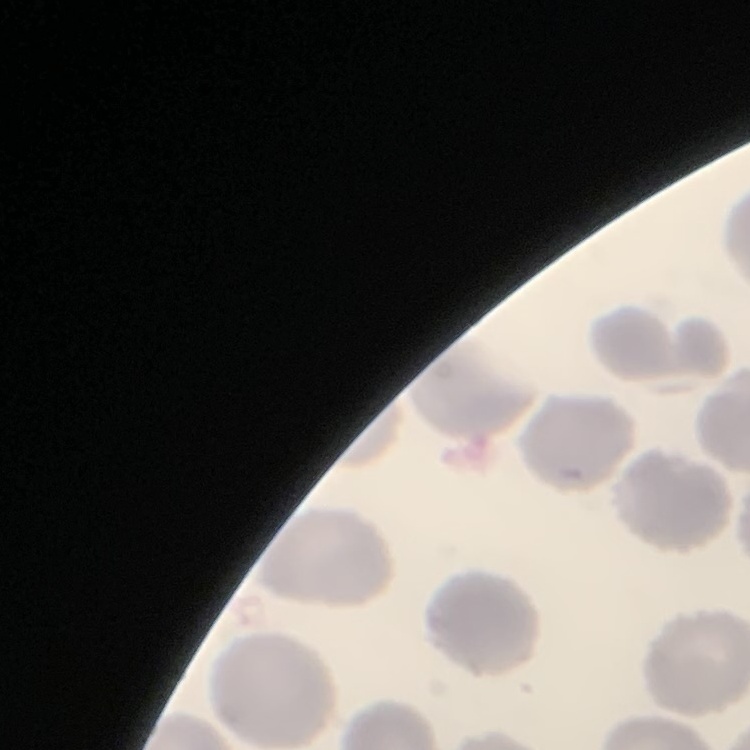
Summary:
  - Erythrocyte morphology: no rouleaux formation
  - Preparation: thin peripheral smear
  - Image type: one tile cut from a larger photomicrograph
  - Stain: Field's or Giemsa